State which parasite is depicted.
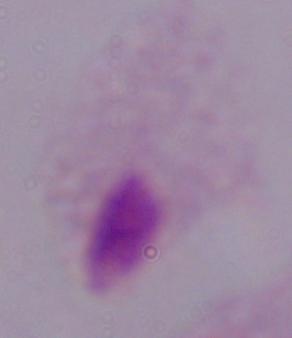

A trichomonad.

magnification = 1000x
modality = photomicrograph